Outline each uninfected red blood cell.
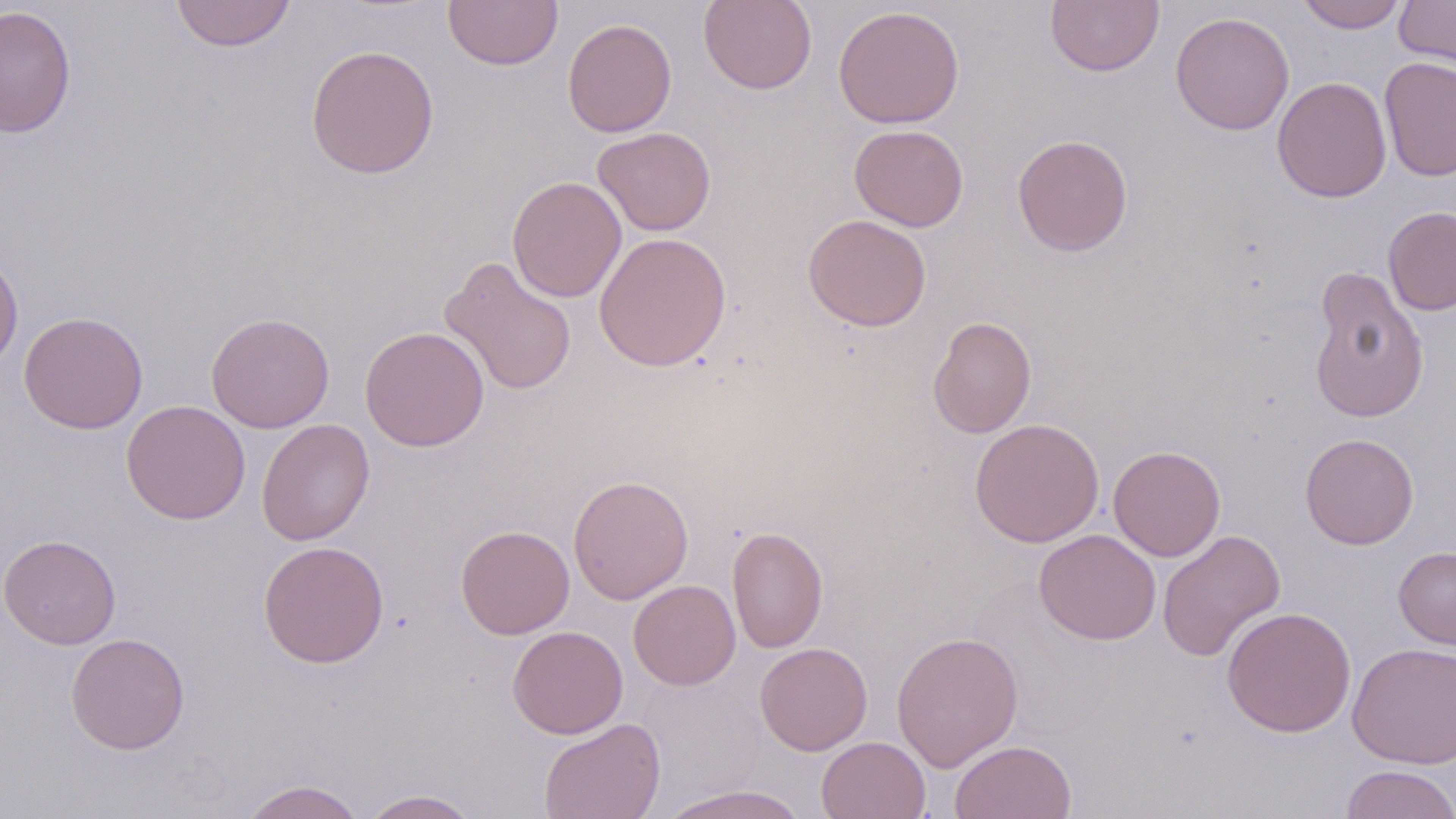
Approximate bounding boxes as (x1, y1, x2, y2) in pixels.
Uninfected red blood cells: (170, 0, 296, 52), (443, 0, 562, 70), (699, 0, 817, 94), (1045, 0, 1164, 77), (1293, 0, 1408, 32), (1395, 0, 1456, 76), (0, 5, 76, 137), (833, 5, 965, 129), (1170, 12, 1295, 135), (562, 18, 677, 137), (306, 43, 439, 180), (1379, 57, 1456, 182), (1272, 76, 1392, 203), (849, 125, 968, 231), (592, 126, 716, 236), (1012, 134, 1133, 256), (506, 176, 627, 303), (1383, 206, 1456, 316), (802, 214, 932, 332), (593, 231, 732, 372), (0, 250, 23, 371), (439, 255, 577, 396), (1307, 265, 1429, 424), (19, 311, 148, 434), (206, 312, 335, 433), (927, 316, 1036, 438), (359, 326, 490, 452), (120, 400, 251, 524), (256, 418, 375, 546), (969, 418, 1105, 547), (1299, 432, 1419, 550), (1108, 445, 1226, 561), (568, 475, 694, 604), (455, 524, 575, 639), (727, 525, 828, 654), (1034, 529, 1161, 645), (1157, 529, 1286, 662), (0, 534, 121, 649), (258, 540, 389, 668), (1393, 546, 1456, 650), (628, 579, 741, 690), (1222, 606, 1357, 737), (507, 625, 628, 739), (891, 630, 1024, 772), (65, 632, 190, 754), (1347, 641, 1456, 768), (755, 642, 873, 756), (538, 717, 666, 819), (816, 736, 930, 818), (949, 740, 1077, 819), (1339, 765, 1456, 819), (238, 779, 367, 819), (658, 784, 808, 819), (360, 789, 480, 819).

slide-level diagnosis = negative for blood parasites
preparation = thin blood film
magnification = 1000x
modality = light microscopy
field of view = single
image size = 1456×819 pixels
stain = May-Grünwald-Giemsa